State which parasite is depicted.
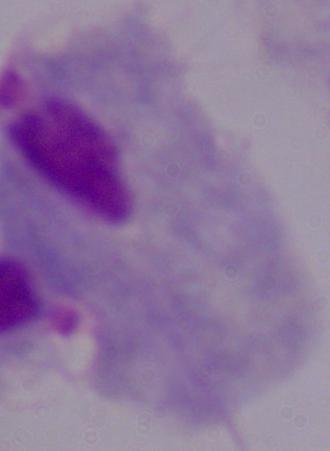

A trichomonad.

Captured at 1000x magnification. Micrograph.